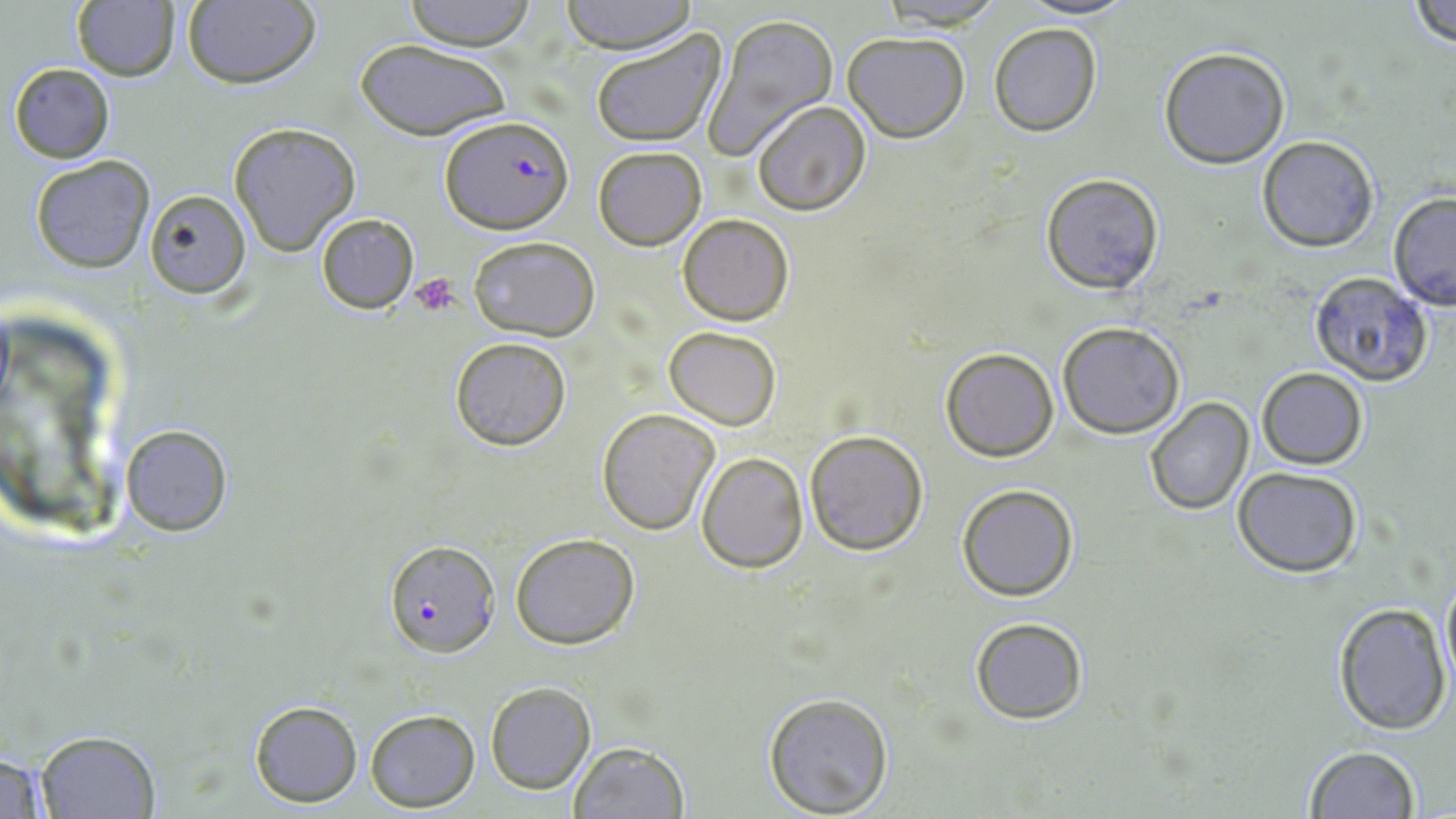
slide-level diagnosis = Plasmodium falciparum
field of view = single
uninfected red blood cell locations = approximate bounding boxes as (x1, y1, x2, y2) in pixels: (181, 0, 320, 89), (403, 0, 537, 49), (560, 0, 696, 54), (1018, 0, 1134, 20), (875, 1, 1008, 30), (1408, 1, 1456, 51), (70, 2, 180, 81), (701, 13, 838, 157), (988, 22, 1101, 136), (590, 26, 727, 149), (842, 31, 970, 142), (354, 38, 513, 142), (1159, 46, 1289, 168), (8, 63, 115, 163), (751, 102, 870, 217), (228, 122, 360, 255), (1257, 135, 1381, 253), (593, 146, 707, 250), (30, 155, 154, 274), (1040, 172, 1165, 294), (145, 188, 251, 298), (1386, 193, 1456, 311), (316, 213, 419, 313), (677, 213, 795, 326), (467, 235, 600, 340), (1307, 273, 1434, 386), (1057, 321, 1186, 438), (663, 326, 781, 430), (449, 336, 571, 451), (939, 347, 1060, 461), (1257, 367, 1367, 469), (1144, 397, 1254, 515), (596, 408, 719, 535), (119, 423, 232, 535), (805, 429, 929, 556), (695, 452, 809, 573), (1234, 467, 1362, 578), (956, 483, 1078, 602), (509, 532, 639, 649), (1440, 567, 1456, 694), (1333, 603, 1452, 735), (968, 615, 1090, 726), (484, 681, 595, 794), (761, 690, 894, 817), (248, 699, 363, 806), (365, 709, 481, 812), (34, 729, 160, 817), (567, 741, 689, 819), (1302, 746, 1420, 819), (0, 747, 53, 818)
modality = optical microscopy
magnification = 1000x
platelet locations = approximate bounding boxes as (x1, y1, x2, y2) in pixels: (411, 274, 461, 317)
preparation = thin blood smear
Plasmodium falciparum-infected red blood cell locations = approximate bounding boxes as (x1, y1, x2, y2) in pixels: (439, 114, 572, 231), (385, 540, 501, 655)
image size = 1456×819 pixels
stain = May-Grünwald-Giemsa